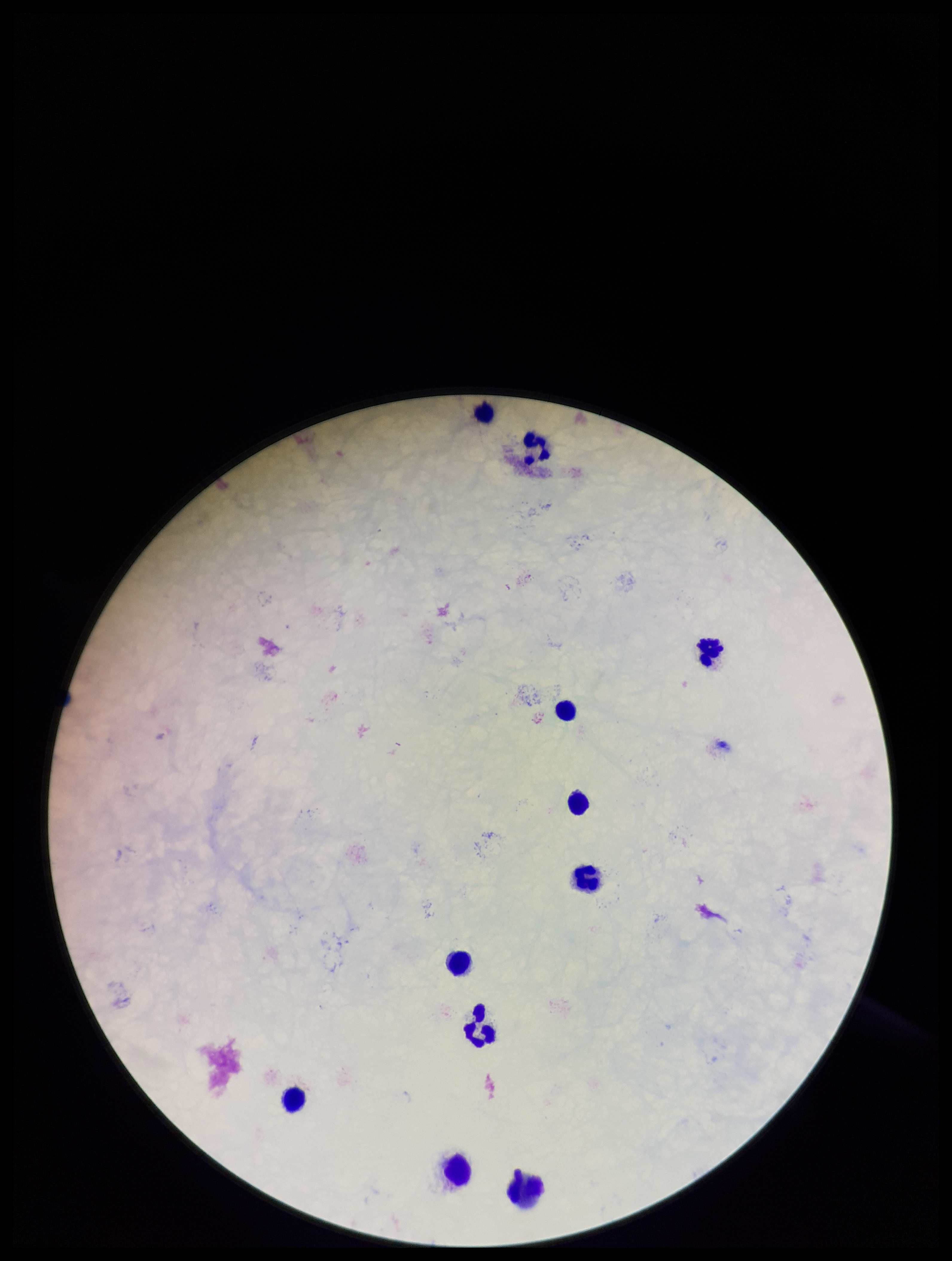

Summary:
  - Capture: smartphone photograph through the microscope eyepiece
  - Image size: 952×1261 pixels
  - Field of view: single
  - Plasmodium parasites: none seen
  - Stain: Giemsa
  - Patient malaria status: negative
  - Leukocyte count: 11
  - Parasite count: 0
  - Preparation: thick